Locate every leukocyte (white blood cell).
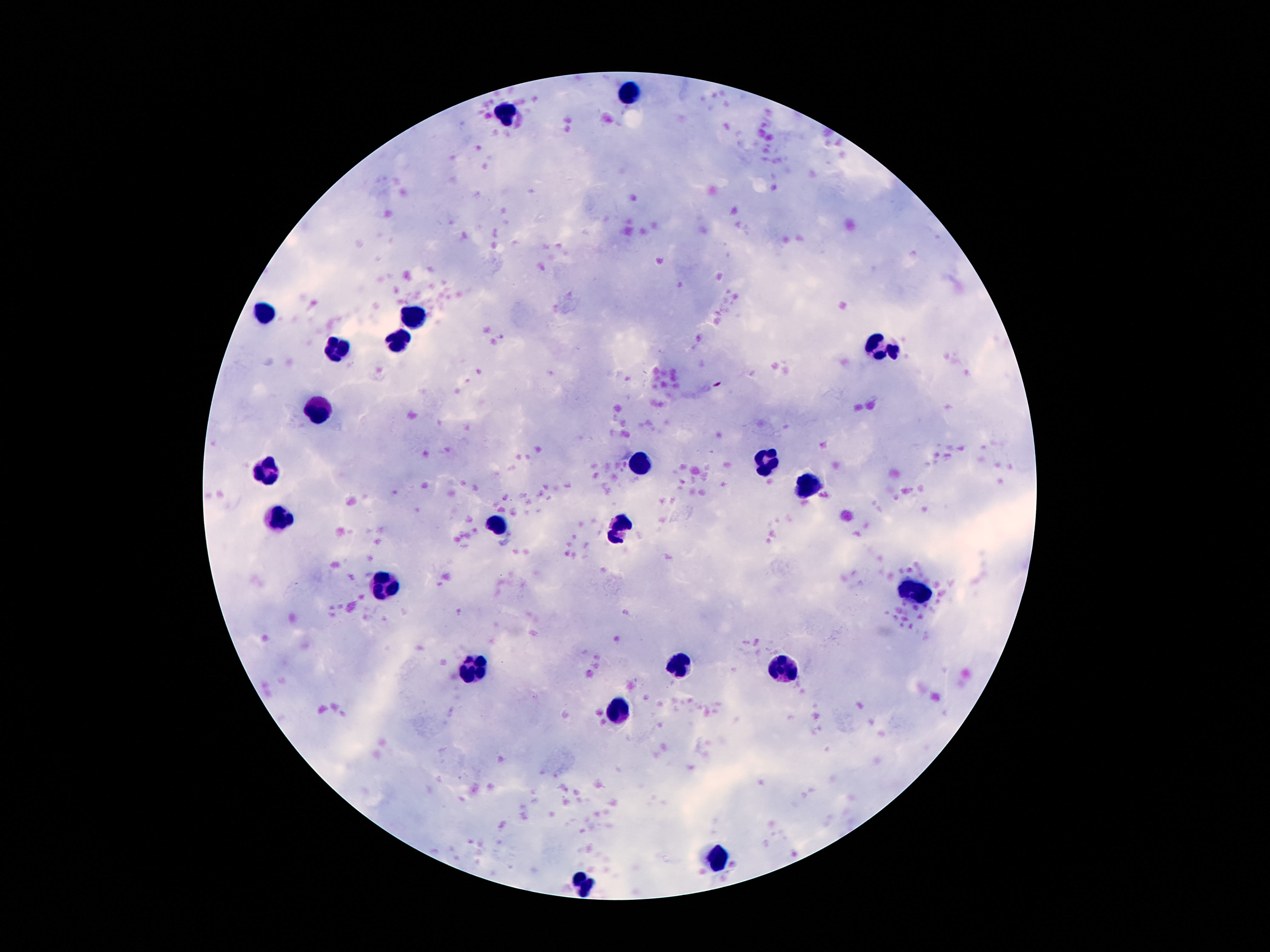
Approximate centers as (x, y) in pixels.
Leukocytes: (628, 94), (505, 109), (263, 312), (412, 312), (400, 337), (876, 345), (337, 351), (316, 409), (639, 463), (767, 463), (269, 470), (809, 484), (280, 519), (498, 527), (622, 531), (391, 585), (914, 593), (677, 665), (475, 667), (782, 667), (618, 711), (719, 853), (582, 884).

magnification = 100x
stain = Giemsa
preparation = thick blood film
capture = smartphone camera through the microscope eyepiece
patient malaria status = negative
image size = 1270×952 pixels
field of view = single